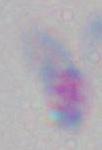
Photomicrograph. Toxoplasma gondii is seen. 1000x magnification.